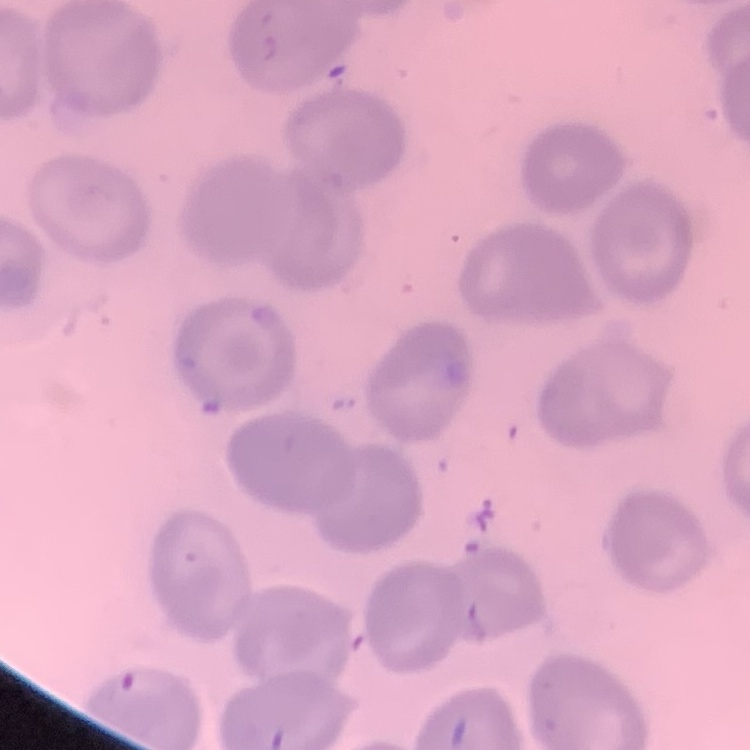

erythrocyte_morphology: no rouleaux formation
image_type: one tile cut from a larger photomicrograph
stain: Field's or Giemsa
preparation: thin blood smear